Locate every leukocyte (white blood cell).
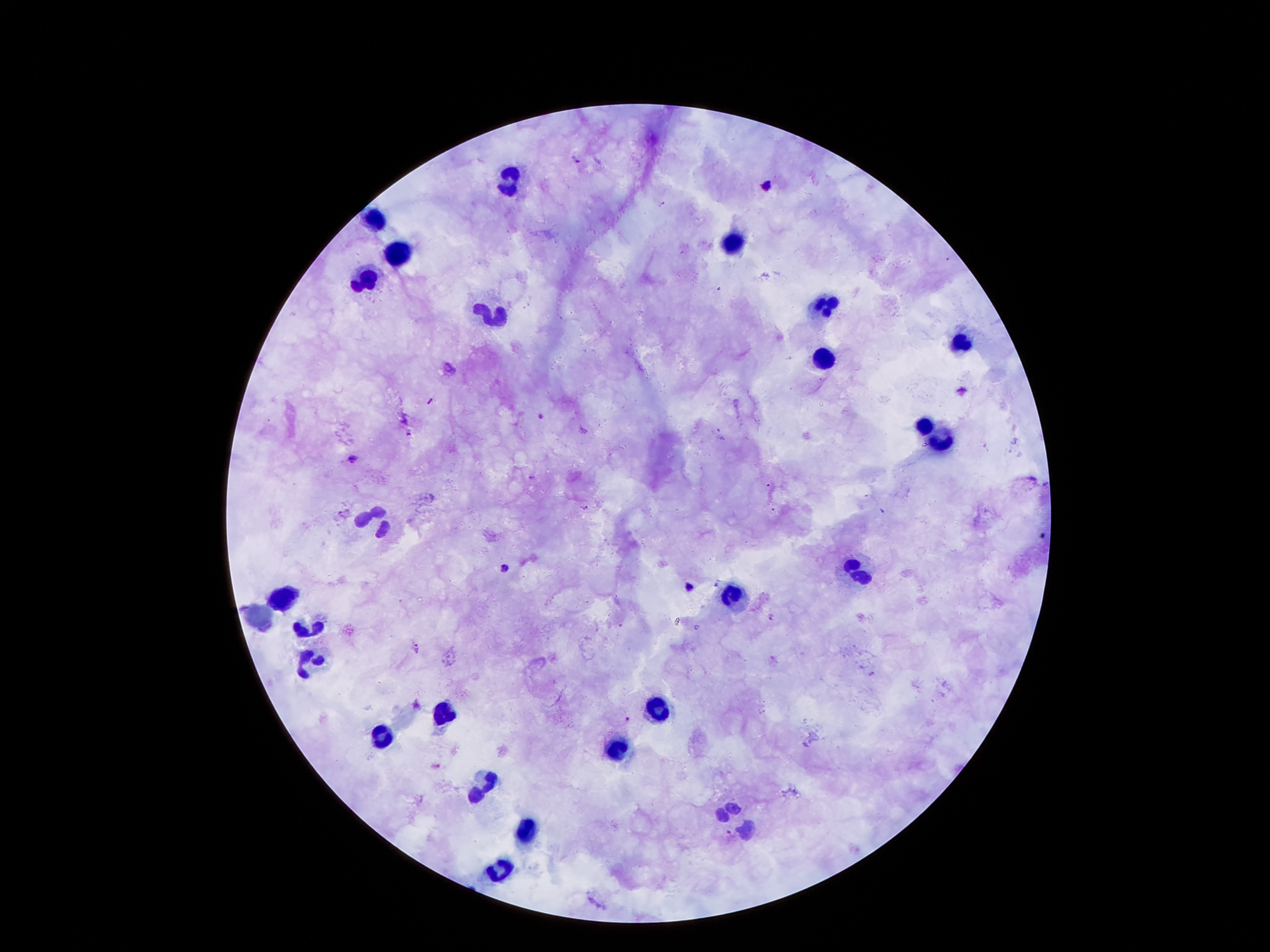

Approximate object centers, in pixels from the top-left corner.
Leukocytes: (x=512, y=176), (x=376, y=217), (x=733, y=242), (x=397, y=254), (x=365, y=279), (x=828, y=304), (x=497, y=316), (x=960, y=340), (x=826, y=358), (x=925, y=426), (x=942, y=441), (x=374, y=522), (x=862, y=571), (x=285, y=599), (x=310, y=629), (x=306, y=662), (x=660, y=712), (x=442, y=714), (x=381, y=737), (x=621, y=748), (x=487, y=785), (x=524, y=830), (x=499, y=872).

plasmodium_parasite_locations: 'approximate object centers, in pixels from the top-left corner: (x=540, y=417), (x=409, y=433), (x=352, y=458), (x=584, y=509), (x=506, y=568), (x=770, y=617), (x=417, y=648), (x=871, y=674), (x=626, y=720), (x=729, y=833)'
capture: smartphone through the microscope eyepiece
stain: Giemsa
preparation: thick peripheral-blood smear
field_of_view: single
magnification: 100x
patient_malaria_status: infected with Plasmodium falciparum
image_size: 1270×952 pixels